Give the position of every Plasmodium parasite.
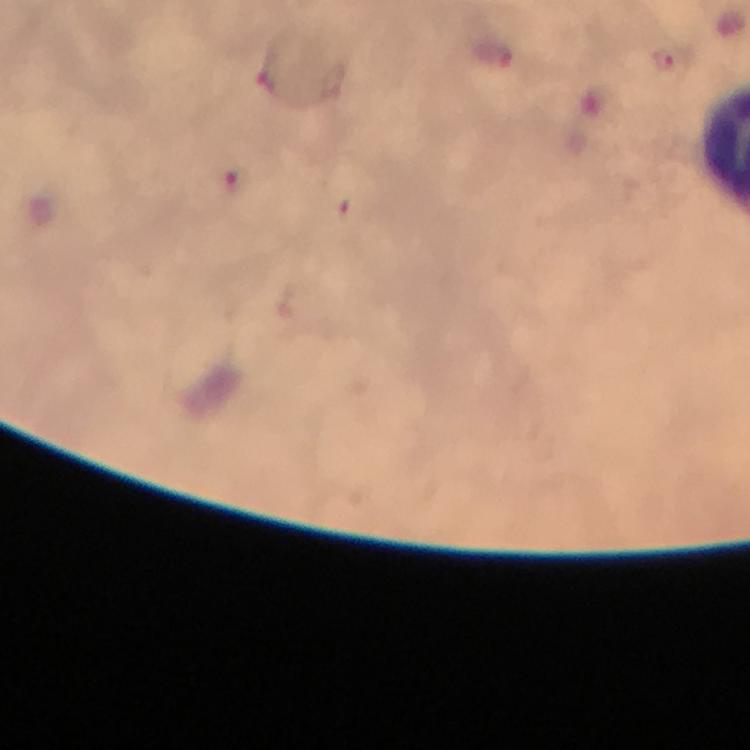
Approximate object centers, in pixels from the top-left corner.
Plasmodium parasites: (x=496, y=57), (x=664, y=62), (x=267, y=76), (x=235, y=178), (x=353, y=212).

Summary:
  - Image size: 750×750 pixels
  - Magnification: 100x
  - Stain: Giemsa
  - Context: from a diagnostic examination for malaria
  - Preparation: thick blood film
  - Immersion oil: applied
  - Capture: smartphone camera through the microscope
  - Cropped from: one field of view